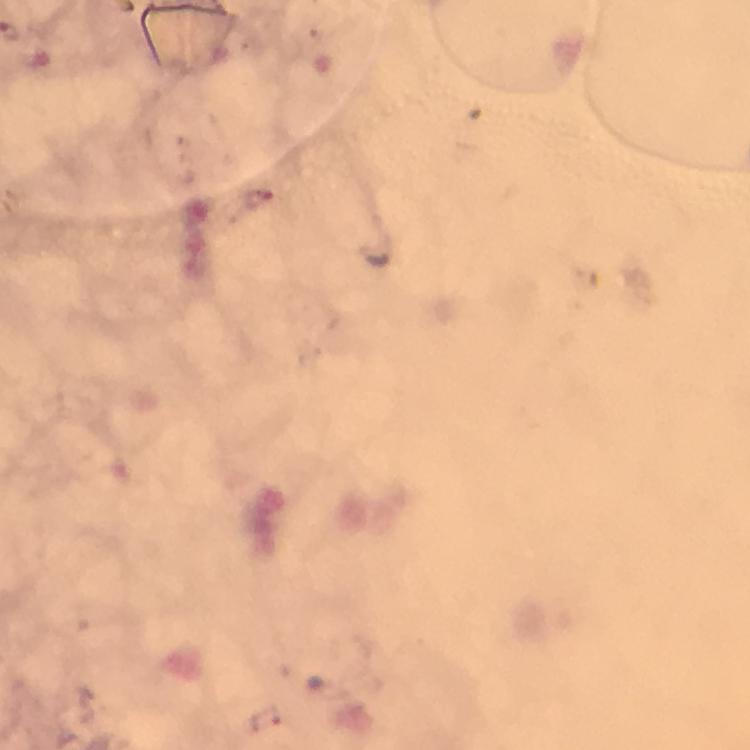

Approximate object centers, in pixels from the top-left corner.
Summary:
  - Malaria parasite locations: (x=260, y=200)
  - Magnification: 100x
  - Capture: smartphone photograph through a microscope
  - Stain: Giemsa
  - Context: from a diagnostic examination for malaria
  - Image size: 750×750 pixels
  - Cropped from: a single field of view
  - Immersion oil: applied
  - Preparation: thick blood film